Name the blood parasite species.
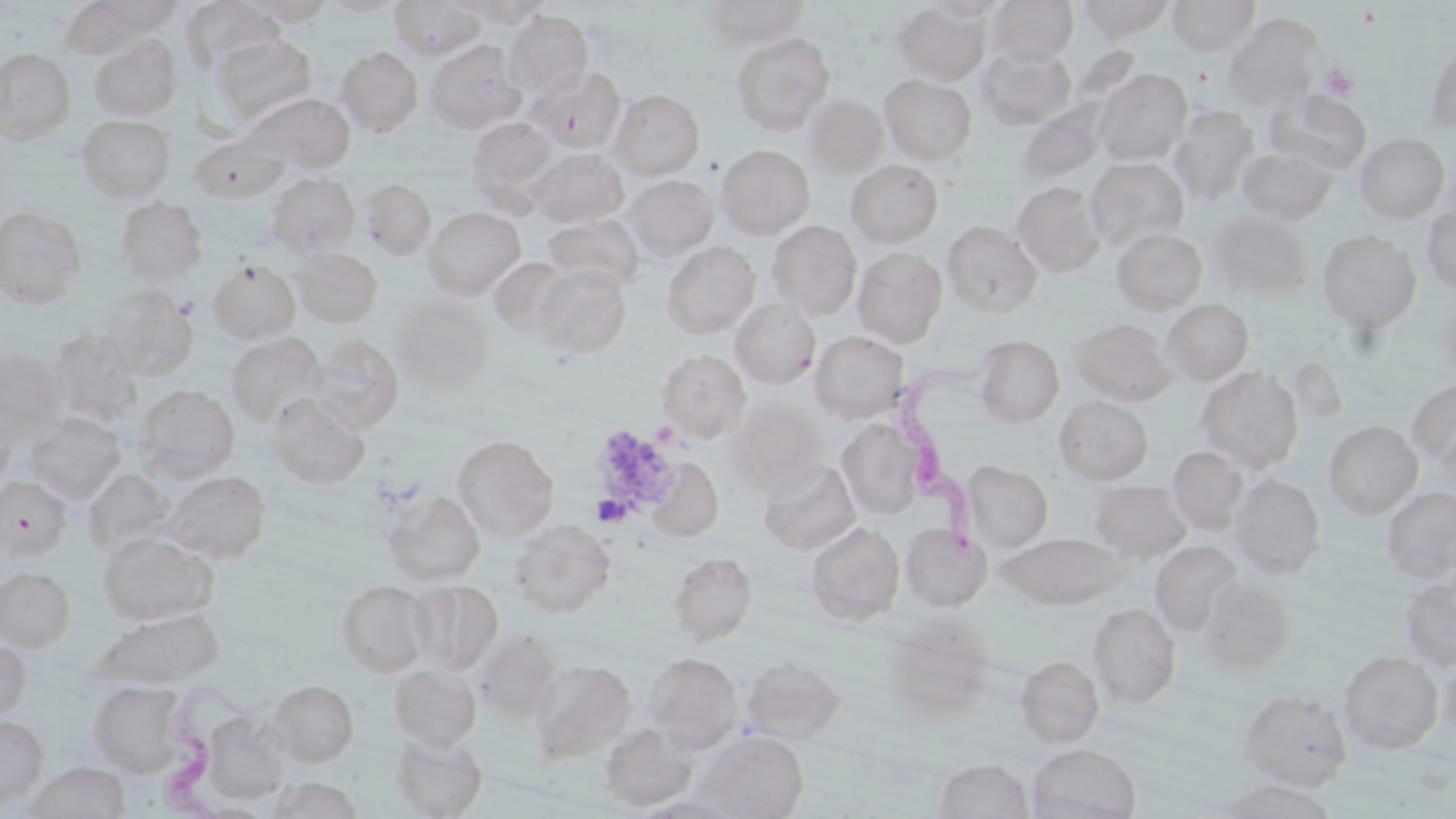
Trypanosoma brucei.

magnification = 1000x
platelet locations = approximate bounding boxes as [x1, y1, x2, y2] in pixels: [1320, 63, 1360, 101], [602, 432, 672, 499], [595, 490, 634, 534]
preparation = thin blood smear
modality = optical microscopy
stain = May-Grünwald-Giemsa
field of view = one of a larger specimen
uninfected red blood cell locations = approximate bounding boxes as [x1, y1, x2, y2] in pixels: [62, 0, 169, 56], [241, 0, 339, 25], [322, 0, 409, 17], [391, 0, 485, 59], [455, 0, 555, 25], [701, 0, 809, 47], [986, 0, 1078, 65], [1076, 0, 1176, 40], [1168, 0, 1259, 55], [181, 1, 284, 75], [892, 1, 991, 85], [923, 1, 1009, 24], [504, 9, 593, 97], [1224, 15, 1323, 108], [730, 32, 835, 134], [90, 35, 181, 120], [211, 35, 317, 122], [425, 40, 525, 131], [1424, 42, 1456, 132], [336, 46, 423, 136], [976, 46, 1076, 129], [0, 48, 74, 141], [525, 64, 626, 152], [1095, 69, 1192, 165], [879, 74, 976, 164], [610, 89, 704, 179], [1265, 89, 1371, 174], [241, 92, 355, 172], [804, 95, 889, 176], [1016, 100, 1109, 183], [1169, 104, 1259, 203], [77, 114, 175, 201], [467, 117, 558, 203], [1354, 133, 1451, 222], [189, 136, 288, 201], [715, 144, 813, 238], [528, 149, 628, 227], [1237, 149, 1337, 223], [1086, 158, 1189, 249], [846, 160, 943, 246], [266, 172, 360, 257], [625, 174, 717, 260], [361, 179, 436, 259], [1011, 182, 1105, 275], [116, 197, 208, 283], [0, 205, 86, 306], [1422, 205, 1456, 293], [423, 207, 525, 298], [1211, 211, 1312, 298], [543, 215, 644, 290], [767, 220, 862, 320], [943, 220, 1043, 316], [1112, 228, 1207, 311], [1317, 230, 1421, 331], [661, 242, 760, 338], [853, 246, 947, 346], [292, 247, 382, 327], [489, 258, 574, 337], [208, 260, 301, 342], [533, 265, 631, 356], [100, 285, 198, 379], [391, 296, 492, 393], [1432, 297, 1456, 377], [730, 298, 821, 388], [1161, 299, 1254, 384], [1073, 319, 1176, 405], [48, 329, 143, 425], [811, 331, 908, 422], [226, 333, 327, 425], [308, 335, 403, 432], [972, 335, 1064, 425], [0, 347, 66, 440], [656, 349, 750, 442], [1196, 367, 1303, 470], [1407, 379, 1456, 470], [135, 384, 240, 478], [267, 394, 370, 488], [1054, 396, 1153, 485], [725, 400, 827, 494], [0, 408, 16, 496], [25, 414, 125, 501], [836, 419, 930, 518], [1323, 421, 1423, 517], [452, 434, 558, 539], [1167, 446, 1248, 533], [647, 458, 723, 542], [758, 459, 860, 554], [963, 460, 1053, 554], [84, 469, 174, 556], [162, 470, 270, 561], [1228, 473, 1325, 577], [0, 476, 71, 558], [1090, 481, 1192, 562], [1382, 486, 1456, 579], [382, 490, 485, 585], [508, 520, 615, 617], [806, 521, 905, 623], [901, 523, 992, 611], [98, 532, 218, 624], [1000, 532, 1127, 609], [1150, 540, 1243, 635], [669, 551, 757, 645], [0, 567, 74, 649], [1399, 575, 1456, 669], [1200, 577, 1295, 673], [410, 580, 502, 672], [336, 581, 430, 675], [1088, 603, 1181, 707], [96, 609, 224, 686], [883, 619, 994, 721], [473, 628, 564, 722], [0, 639, 30, 719], [1337, 651, 1444, 753], [644, 652, 741, 751], [1437, 652, 1456, 743], [741, 655, 845, 745], [1015, 655, 1104, 747], [531, 660, 635, 762], [389, 665, 481, 750], [90, 680, 185, 776], [269, 680, 359, 766], [1238, 688, 1352, 790], [196, 708, 292, 806], [0, 716, 47, 806], [599, 723, 698, 811], [696, 731, 809, 819], [390, 734, 487, 818], [1027, 743, 1141, 819], [934, 758, 1032, 818], [27, 762, 129, 819], [267, 776, 364, 818], [1217, 780, 1341, 818]
image size = 1456×819 pixels
Trypanosoma brucei locations = approximate bounding boxes as [x1, y1, x2, y2] in pixels: [885, 340, 995, 562], [159, 672, 271, 818]